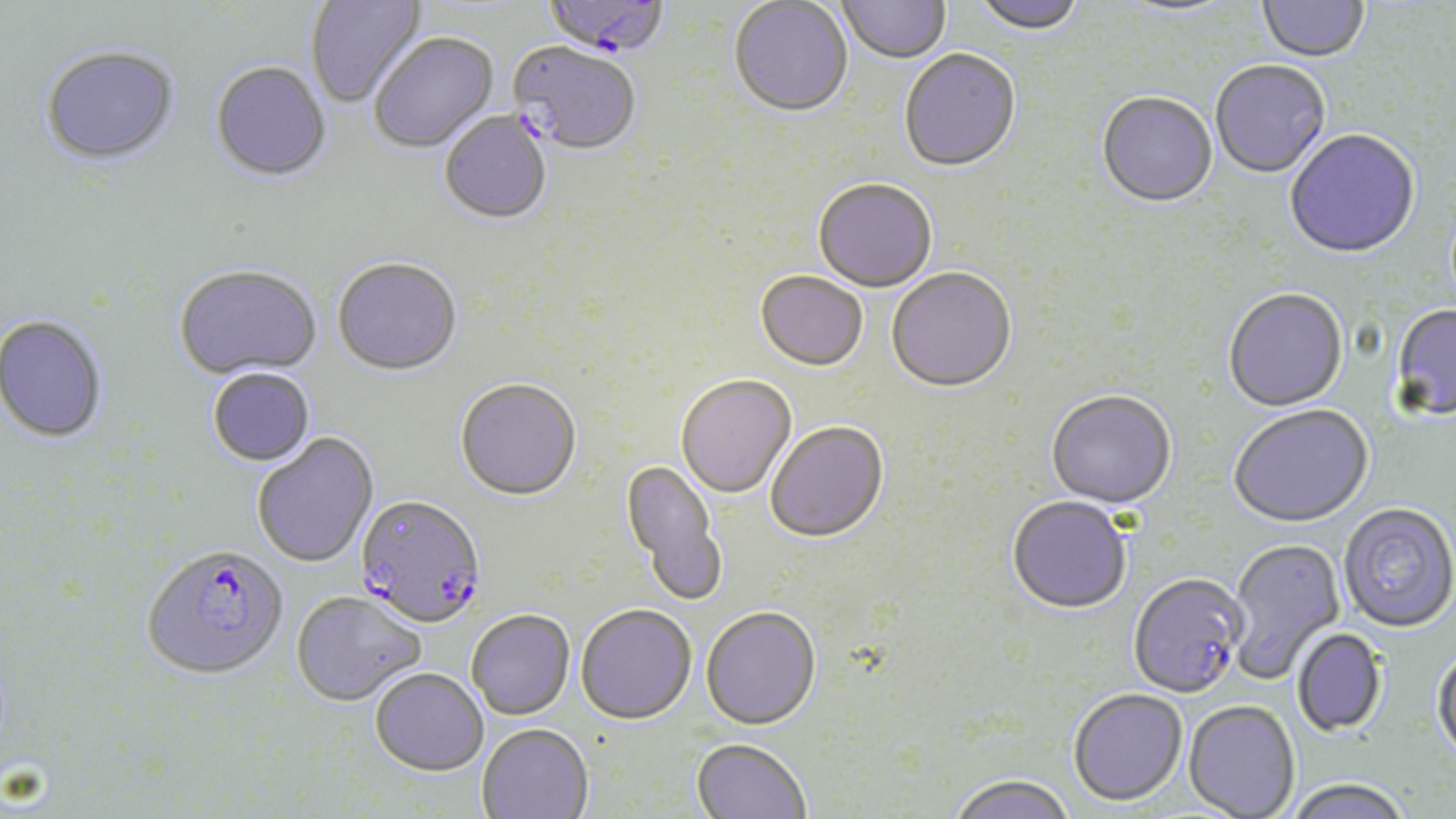
Summary:
  - Coordinate format: approximate bounding boxes as (x1,y1)-(x2,y2) corner pairs in pixels
  - Plasmodium falciparum-infected red blood cell locations: (542,0)-(669,62), (508,44)-(641,158), (355,497)-(488,631), (141,546)-(288,682), (1128,574)-(1248,700)
  - Uninfected red blood cell locations: (306,0)-(429,110), (837,0)-(951,66), (970,0)-(1087,37), (1257,0)-(1369,65), (729,1)-(853,120), (1113,1)-(1242,19), (369,35)-(500,156), (40,49)-(180,169), (899,51)-(1021,175), (1210,61)-(1331,180), (211,63)-(331,184), (1096,93)-(1217,210), (440,113)-(552,226), (1284,130)-(1421,261), (813,181)-(937,294), (332,261)-(463,379), (175,267)-(322,381), (886,270)-(1016,396), (755,272)-(868,373), (1223,290)-(1349,414), (1390,305)-(1456,423), (0,315)-(108,444), (207,369)-(316,468), (676,376)-(797,500), (455,380)-(582,504), (1046,392)-(1177,511), (1229,406)-(1374,530), (765,423)-(889,546), (253,433)-(379,569), (619,459)-(727,607), (1007,498)-(1132,616), (1338,504)-(1456,635), (1225,538)-(1346,684), (292,593)-(425,708), (576,606)-(697,727), (700,608)-(821,732), (467,611)-(575,721), (1292,629)-(1388,737), (1431,648)-(1456,767), (371,669)-(488,776), (1068,690)-(1188,809), (1183,702)-(1300,819), (477,725)-(593,819), (691,739)-(811,819), (947,776)-(1076,819), (1284,780)-(1411,819)
  - Slide-level diagnosis: Plasmodium falciparum
  - Field of view: one of a larger specimen
  - Preparation: thin blood film
  - Modality: optical microscopy
  - Image size: 1456×819 pixels
  - Stain: May-Grünwald-Giemsa
  - Magnification: 1000x